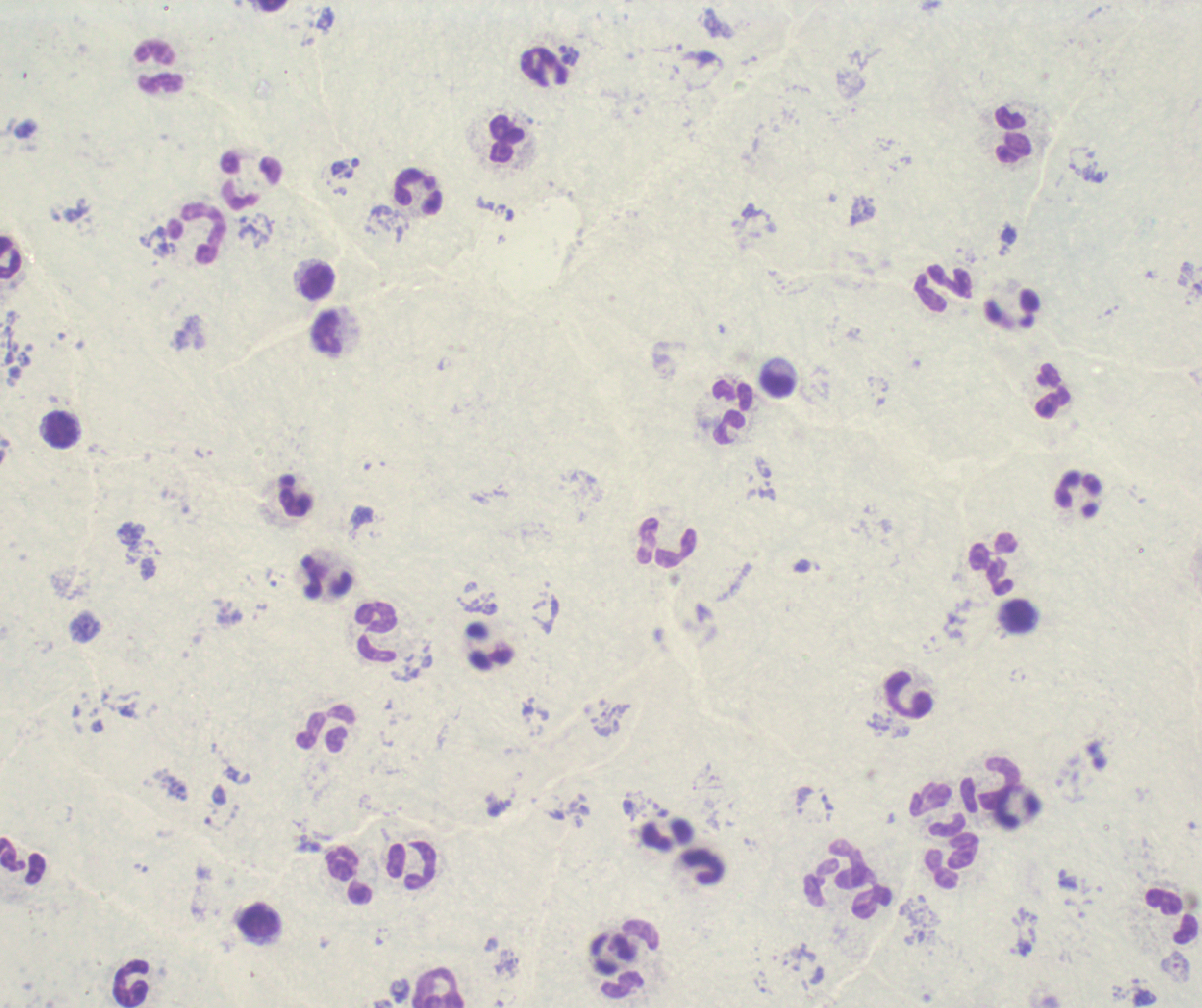

coordinate format = approximate centers as (x, y) in pixels
leukocyte locations = (272, 5), (161, 68), (1013, 135), (505, 139), (252, 180), (418, 191), (197, 235), (10, 257), (317, 281), (943, 289), (327, 333), (776, 382), (1052, 390), (733, 412), (62, 430), (296, 495), (1078, 495), (667, 543), (994, 564), (326, 576), (1020, 617), (376, 633), (908, 696), (326, 729), (990, 783), (938, 808), (22, 861), (951, 861), (341, 863), (411, 865), (703, 866), (859, 894), (1172, 917), (260, 922), (611, 954), (131, 984), (439, 989)
trophozoite locations = (569, 55)
field of view = single
context = previously used in an actual diagnosis
background quality = unsatisfactory
preparation = thick blood film
image size = 1202×1008 pixels
result = positive for malaria parasites
stain = Romanowsky
magnification = 100x